Report the malaria status of this cell.
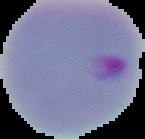

It is parasitized.

Image is 145×139 pixels. From a thin blood smear. Segmented cell region on a black background.